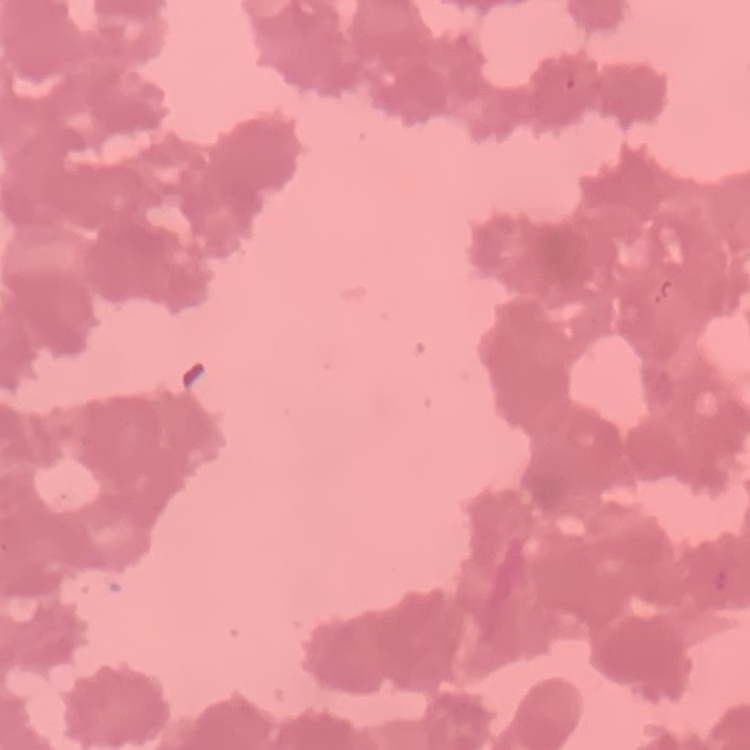

Summary:
  - Erythrocyte morphology: rouleaux formation
  - Stain: Field's or Giemsa
  - Image type: one tile cut from a larger photomicrograph
  - Preparation: thin blood smear